Assess this cell for malaria.
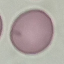

Uninfected.

Photographed with a smartphone camera at the microscope eyepiece. Thin blood smear. Cell patch, automatically extracted from a larger field of view and resized to 64 × 64 pixels. Giemsa-stained preparation.